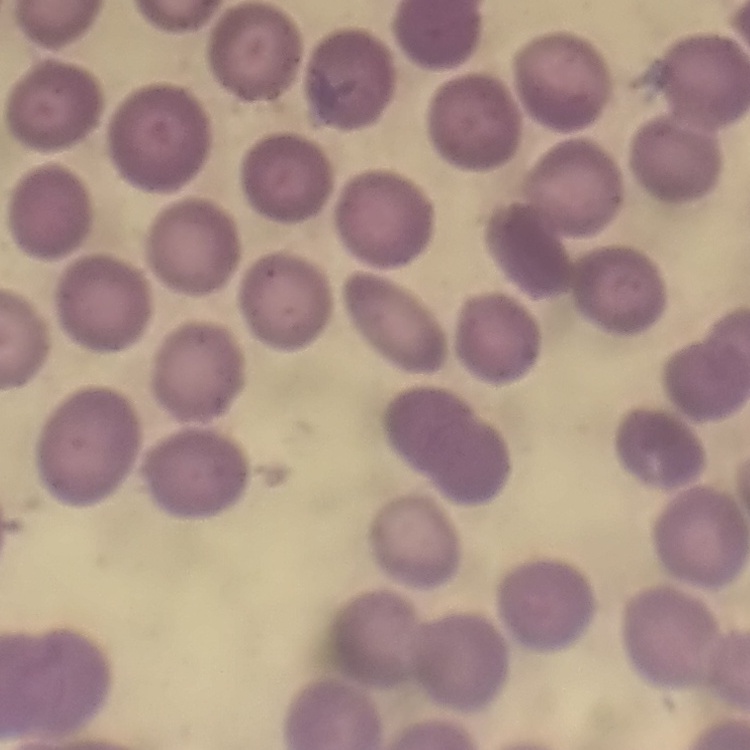

Summary:
  - Erythrocyte morphology: no rouleaux formation
  - Preparation: thin blood film
  - Stain: Field's or Giemsa
  - Image type: square crop of a larger photomicrograph